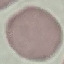
Result: negative for malaria parasites. Photographed with a smartphone camera at the microscope eyepiece. Cell patch, automatically extracted from a larger field of view and resized to 64 × 64 pixels. Giemsa stain. Thin blood smear.